Give the position of every malaria parasite.
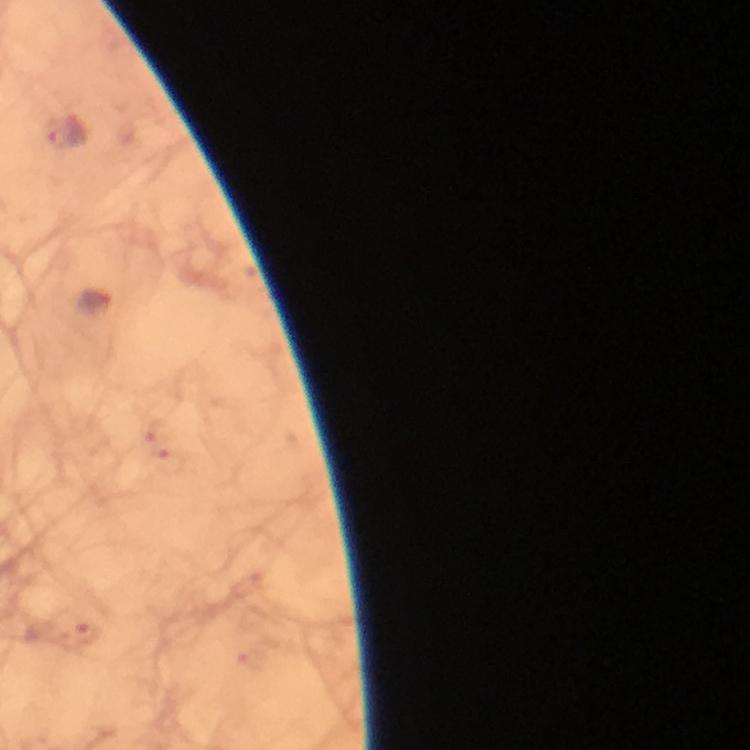
Approximate centers as [x, y] in pixels.
Malaria parasites: [66, 134], [97, 305].

From a diagnostic examination for malaria. Image is 750×750 pixels. 100x magnification. Photographed with a smartphone mounted on the microscope. A crop from one field of view. Immersion oil applied. Giemsa-stained preparation. Thick blood film.